Give the extent of all Plasmodium falciparum-infected red blood cells.
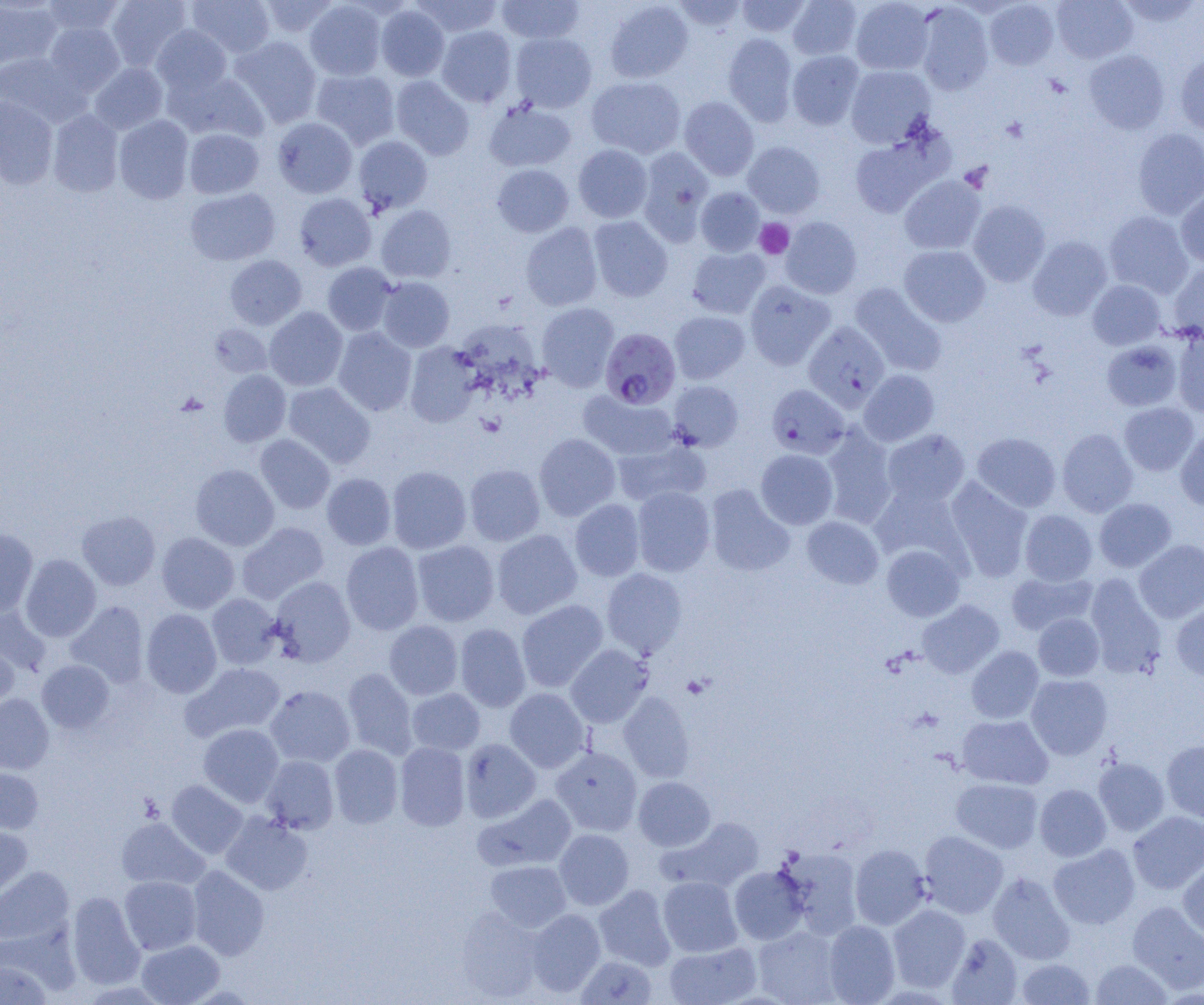

Approximate bounding boxes as (x1, y1, x2, y2) in pixels.
Plasmodium falciparum-infected red blood cells (subset): (601, 327, 681, 409), (766, 384, 849, 459).

{
  "slide_level_diagnosis": "Plasmodium falciparum",
  "image_size": "1204×1005 pixels",
  "uninfected_red_blood_cell_locations_subset": "approximate bounding boxes as (x1, y1, x2, y2) in pixels: (41, 0, 126, 38), (106, 0, 192, 71), (187, 0, 274, 58), (256, 0, 339, 39), (412, 0, 503, 38), (496, 0, 584, 44), (736, 0, 811, 37), (788, 0, 862, 60), (850, 0, 934, 75), (1051, 0, 1138, 64), (1115, 0, 1203, 28), (0, 1, 62, 70), (304, 1, 387, 80), (604, 1, 694, 83), (673, 1, 748, 33), (984, 1, 1059, 70), (914, 2, 994, 95), (376, 5, 450, 81), (44, 22, 125, 96), (151, 25, 232, 96), (436, 25, 517, 107), (510, 32, 597, 113), (723, 33, 798, 125), (231, 36, 322, 126), (787, 50, 864, 129), (1084, 50, 1170, 134), (0, 52, 85, 126), (1176, 54, 1204, 137), (89, 62, 168, 134), (846, 65, 936, 147), (311, 69, 400, 149), (167, 70, 270, 143), (391, 75, 474, 159), (586, 76, 686, 158), (0, 95, 58, 189), (679, 96, 759, 181), (484, 99, 577, 172), (47, 109, 124, 197), (114, 115, 194, 203), (272, 117, 357, 198), (184, 128, 264, 199), (1132, 128, 1204, 219), (850, 133, 946, 218), (353, 135, 433, 214), (742, 141, 825, 218), (573, 144, 653, 222), (636, 147, 714, 244), (492, 164, 574, 237), (899, 175, 986, 255), (695, 187, 765, 256), (185, 188, 280, 265), (1176, 189, 1204, 267), (294, 193, 376, 271), (968, 200, 1050, 287), (375, 205, 456, 283), (1103, 211, 1193, 298), (588, 215, 673, 302), (780, 216, 862, 299), (520, 222, 603, 310), (1028, 236, 1112, 320), (899, 245, 990, 326), (687, 247, 770, 318), (225, 255, 306, 330), (1168, 261, 1204, 340), (322, 262, 397, 336), (377, 277, 455, 352), (744, 280, 835, 370), (1087, 280, 1166, 350), (850, 283, 948, 377), (537, 301, 619, 390), (264, 306, 347, 391), (669, 311, 750, 384), (208, 323, 272, 378), (456, 326, 546, 389), (333, 327, 417, 416), (1171, 330, 1204, 417), (1101, 340, 1182, 411), (405, 341, 481, 427), (219, 369, 291, 446), (859, 369, 939, 446), (668, 380, 743, 451), (283, 382, 375, 468), (578, 390, 678, 461), (1119, 402, 1199, 475), (1175, 425, 1204, 510), (820, 427, 897, 528), (1057, 428, 1138, 517), (882, 429, 970, 507), (972, 432, 1061, 512), (534, 433, 621, 520), (255, 434, 335, 513), (612, 440, 708, 507), (755, 449, 838, 529), (190, 464, 279, 550), (464, 464, 545, 546), (387, 466, 472, 554), (322, 473, 396, 550), (945, 478, 1034, 581), (871, 483, 966, 564), (705, 484, 795, 576), (631, 486, 715, 576), (1094, 498, 1176, 572), (570, 499, 645, 581), (1020, 509, 1097, 585), (77, 511, 160, 590), (801, 516, 884, 589), (237, 522, 328, 603), (0, 528, 38, 616), (492, 529, 582, 619), (157, 532, 239, 614), (1134, 539, 1204, 623), (412, 540, 500, 626), (341, 542, 424, 635), (881, 544, 965, 621), (20, 554, 101, 641), (601, 568, 687, 658), (1006, 571, 1097, 635), (1085, 574, 1167, 678), (269, 576, 355, 667), (207, 593, 283, 670), (516, 599, 608, 691), (917, 600, 1004, 678), (65, 601, 149, 688), (1170, 602, 1204, 681), (0, 606, 51, 675), (141, 609, 221, 698), (1033, 613, 1104, 681), (384, 621, 463, 700), (455, 623, 531, 712), (0, 638, 19, 710), (566, 644, 653, 727), (966, 646, 1044, 723), (37, 660, 114, 732), (182, 662, 286, 742), (342, 667, 418, 760), (1026, 674, 1112, 759), (265, 685, 355, 767), (407, 688, 485, 755), (505, 688, 590, 772), (618, 691, 695, 782), (0, 694, 54, 774), (957, 715, 1053, 789), (198, 723, 284, 807), (460, 738, 541, 823), (1162, 740, 1204, 823), (394, 742, 470, 831), (329, 744, 403, 828), (550, 746, 642, 836), (261, 755, 339, 834), (1093, 757, 1170, 836), (0, 767, 43, 834), (633, 776, 715, 851), (951, 778, 1043, 853), (166, 780, 248, 859), (1034, 784, 1111, 861), (474, 793, 577, 872), (220, 811, 312, 895), (1128, 811, 1204, 894), (116, 817, 209, 890), (660, 817, 764, 892), (0, 826, 33, 899), (554, 829, 634, 910), (920, 831, 1009, 918), (850, 844, 931, 930), (1048, 844, 1140, 929), (778, 848, 863, 939), (1178, 858, 1204, 944), (485, 860, 571, 932), (0, 865, 75, 946), (187, 865, 269, 960), (729, 866, 809, 945), (988, 872, 1076, 965), (119, 875, 201, 955), (658, 876, 743, 957), (593, 885, 675, 971), (67, 891, 145, 989), (1127, 901, 1204, 993), (887, 904, 970, 992), (456, 907, 545, 1002), (526, 909, 605, 997), (823, 920, 900, 1005), (753, 926, 844, 1005), (946, 934, 1022, 1004), (137, 939, 224, 1004), (664, 941, 761, 1005), (575, 955, 657, 1005), (1015, 958, 1095, 1005), (1090, 959, 1173, 1004), (0, 960, 52, 1005)",
  "platelet_locations": "approximate bounding boxes as (x1, y1, x2, y2) in pixels: (755, 219, 794, 259), (683, 675, 711, 699)",
  "field_of_view": "single",
  "modality": "optical microscopy",
  "preparation": "thin blood film",
  "magnification": "1000x"
}